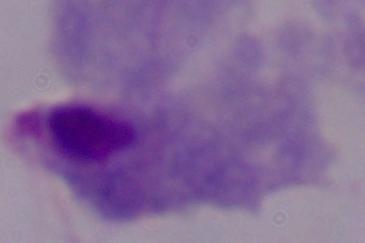

magnification = 1000x
modality = photomicrograph
identification = trichomonad